Identify the parasite.
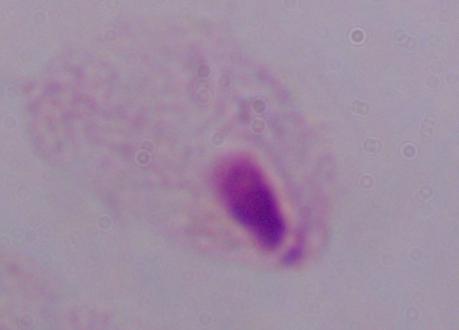

A trichomonad.

Summary:
  - Magnification: 1000x
  - Modality: photomicrograph